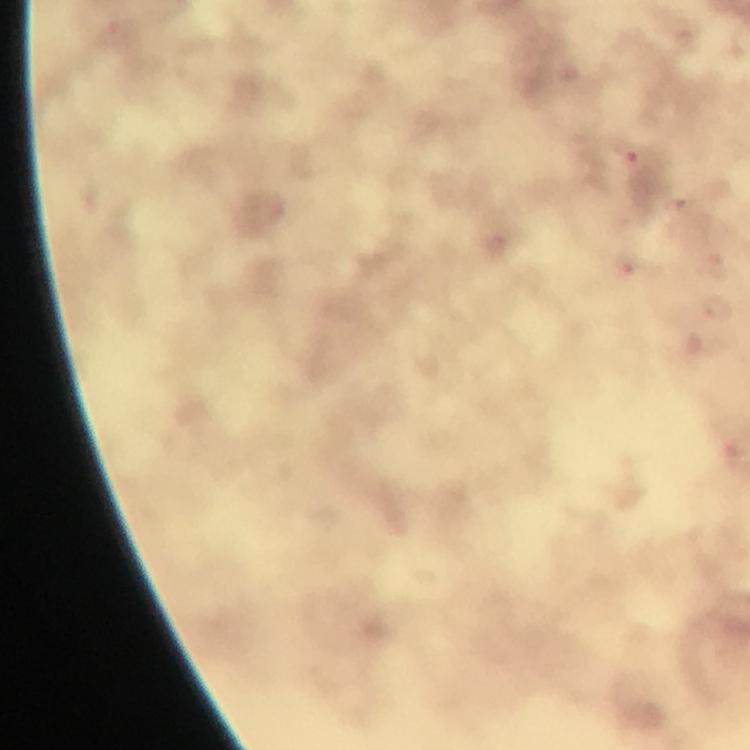

cropped from = one field of view
immersion oil = used
malaria parasite locations = approximate centers as (x, y) in pixels: (629, 151)
context = from a malaria diagnostic workup
magnification = 100x
preparation = thick smear
stain = Giemsa
capture = smartphone photograph through a microscope
image size = 750×750 pixels